Give the position of every P. falciparum parasite, noting its life-cycle stage.
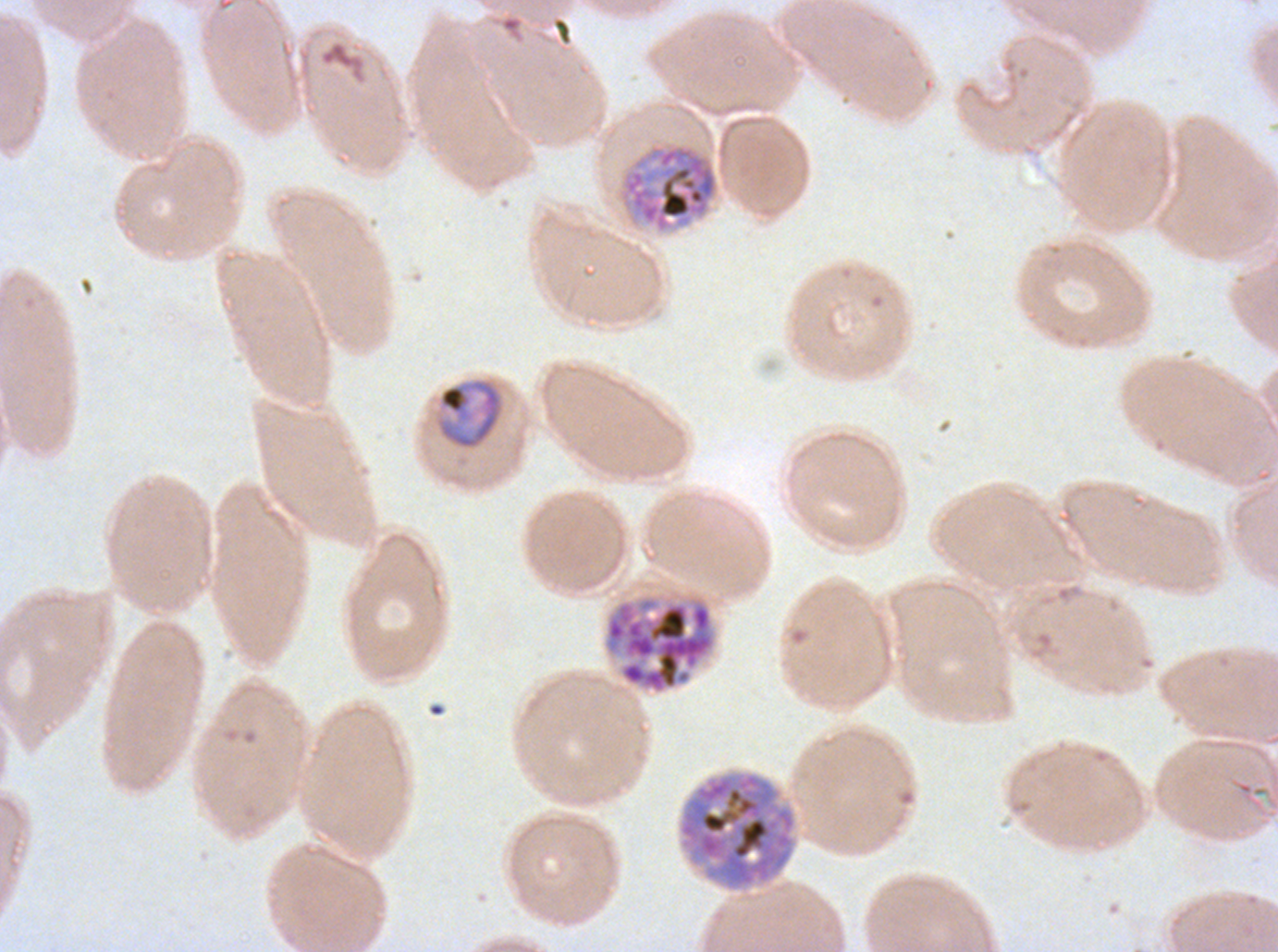
Approximate bounding boxes as [x1, y1, x2, y2] in pixels.
Late trophozoites: [436, 377, 504, 450].
Early schizonts: [619, 143, 719, 234].
Late schizonts: [603, 595, 717, 695], [677, 771, 797, 891].
No rings, late-ring/early-trophozoite forms, mid trophozoites, segmenters, or gametocytes observed.

Giemsa-stained preparation. Thin blood film. A sub-image separated from a larger composite. Life-cycle stages observed: late trophozoite, early schizont, late schizont. Image is 1278×952 pixels. P. falciparum cultured ex vivo for 24 to 48 hours, from a patient in The Gambia.